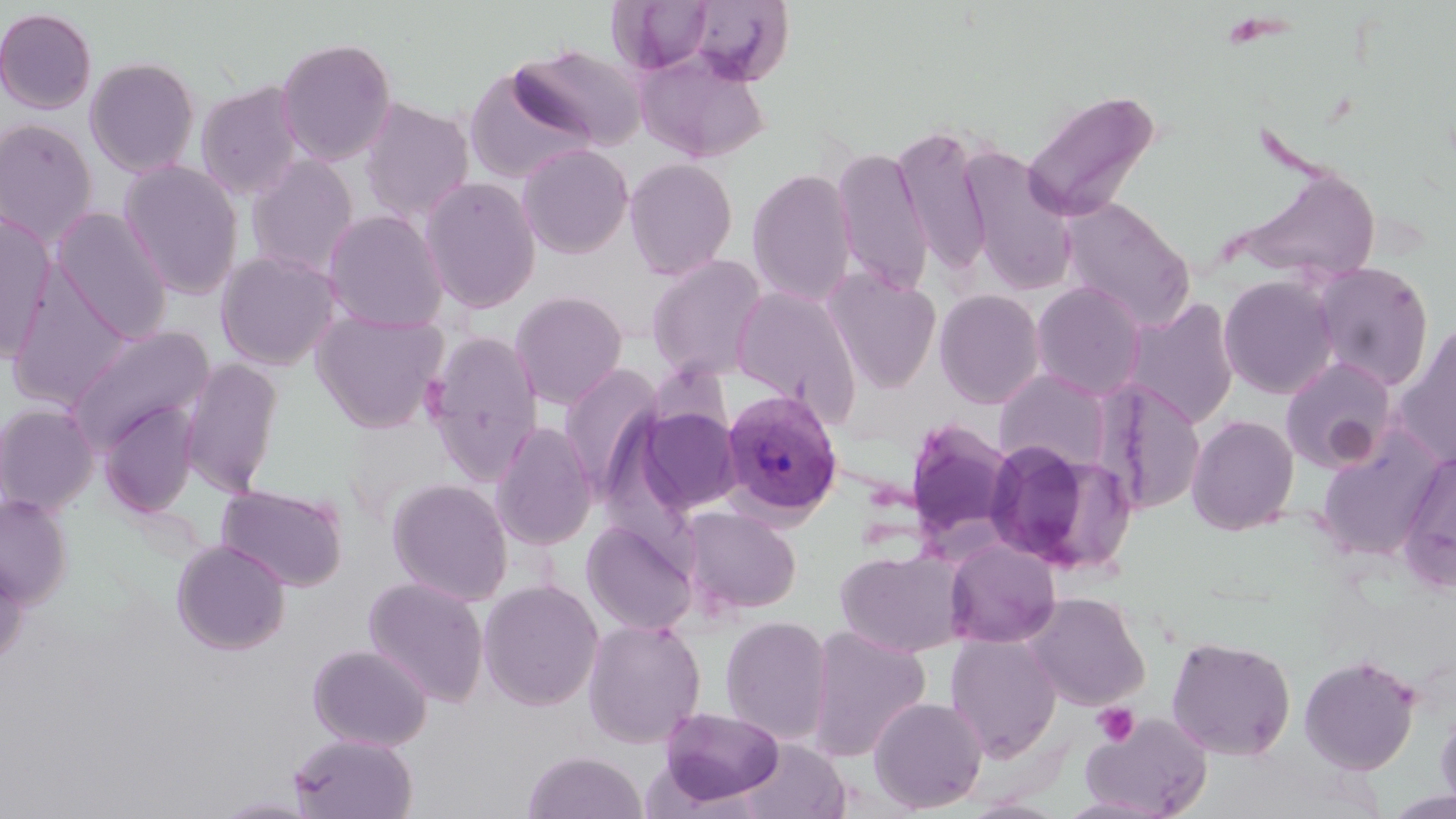

Plasmodium vivax-infected red blood cell locations = approximate bounding boxes as (x1,y1)-(x2,y2) corner pairs in pixels: (721,388)-(843,522)
slide-level diagnosis = Plasmodium vivax
field of view = one of a larger specimen
uninfected red blood cell locations = approximate bounding boxes as (x1,y1)-(x2,y2) corner pairs in pixels: (679,0)-(796,87), (0,7)-(98,114), (275,36)-(397,166), (512,43)-(647,151), (635,49)-(770,163), (84,56)-(200,177), (463,65)-(597,184), (195,81)-(305,200), (1022,88)-(1161,224), (359,97)-(475,223), (0,118)-(99,245), (893,124)-(994,276), (517,143)-(635,259), (831,145)-(933,295), (959,145)-(1077,295), (246,154)-(360,278), (624,157)-(739,280), (118,160)-(244,299), (1236,167)-(1382,282), (746,168)-(857,307), (420,176)-(542,314), (1060,198)-(1196,330), (52,207)-(173,343), (322,209)-(449,332), (0,213)-(56,363), (215,250)-(341,371), (645,253)-(768,381), (1310,262)-(1434,391), (5,266)-(133,411), (823,268)-(942,393), (1218,274)-(1339,399), (1031,281)-(1147,399), (731,285)-(863,420), (934,288)-(1046,409), (510,290)-(628,409), (1125,298)-(1241,429), (311,309)-(448,433), (1393,323)-(1456,468), (63,324)-(217,452), (422,331)-(544,482), (1279,355)-(1399,473), (180,357)-(284,497), (558,363)-(665,495), (994,369)-(1114,473), (1098,380)-(1207,515), (99,401)-(200,518), (0,403)-(99,515), (632,405)-(744,516), (1186,415)-(1299,535), (904,416)-(1017,549), (489,421)-(598,551), (1316,433)-(1442,563), (983,440)-(1132,575), (1397,450)-(1456,591), (387,478)-(514,606), (216,483)-(349,592), (0,494)-(72,606), (680,506)-(802,616), (581,519)-(700,636), (945,538)-(1062,648), (171,539)-(291,655), (834,546)-(967,657), (0,550)-(30,664), (363,577)-(489,707), (479,578)-(604,711), (1023,591)-(1150,709), (719,615)-(834,745), (582,618)-(706,748), (805,626)-(931,763), (946,633)-(1062,761), (1166,636)-(1296,761), (307,643)-(433,750), (1299,653)-(1421,775), (869,696)-(988,814), (1435,704)-(1456,813), (656,706)-(786,809), (1081,713)-(1211,819), (289,733)-(418,818), (738,738)-(850,819), (523,750)-(648,818), (213,796)-(320,818)
image size = 1456×819 pixels
stain = May-Grünwald-Giemsa
preparation = thin blood smear
magnification = 1000x
modality = optical microscopy
platelet locations = approximate bounding boxes as (x1,y1)-(x2,y2) corner pairs in pixels: (1092,703)-(1139,747)